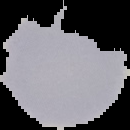

Summary:
  - Result: no Plasmodium parasites detected
  - Image size: 130×130 pixels
  - Image type: cell region segmented out of the field of view; surrounding area masked to black
  - Preparation: thin blood smear